Locate Plasmodium parasites and leukocytes.
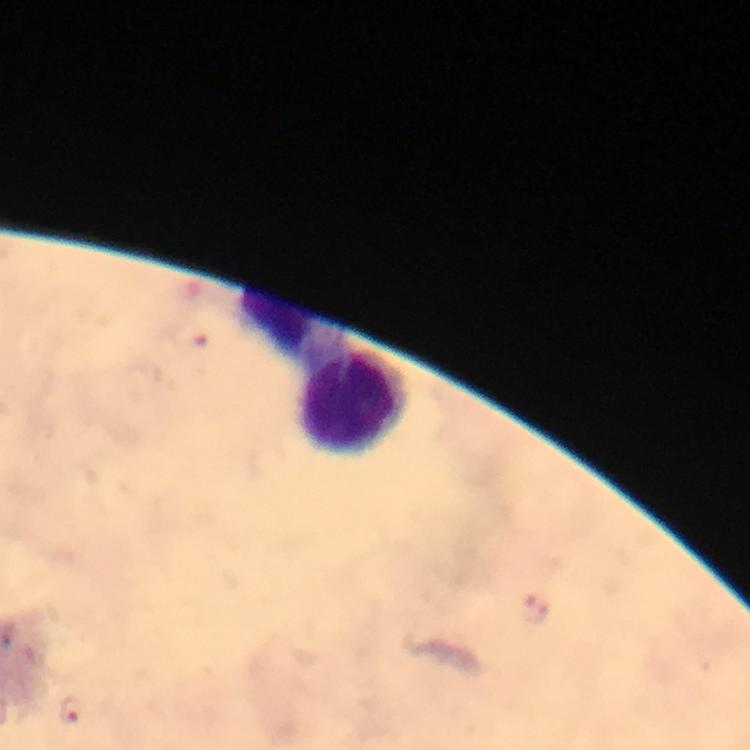

Approximate centers as [x, y] in pixels.
Plasmodium parasites: [73, 711].
Leukocytes: [295, 324], [357, 401].

capture: smartphone camera through the microscope
cropped_from: a single field of view
immersion_oil: applied
stain: Giemsa
context: from a diagnostic examination for malaria
image_size: 750×750 pixels
magnification: 100x
preparation: thick blood film